Comment on the background quality.
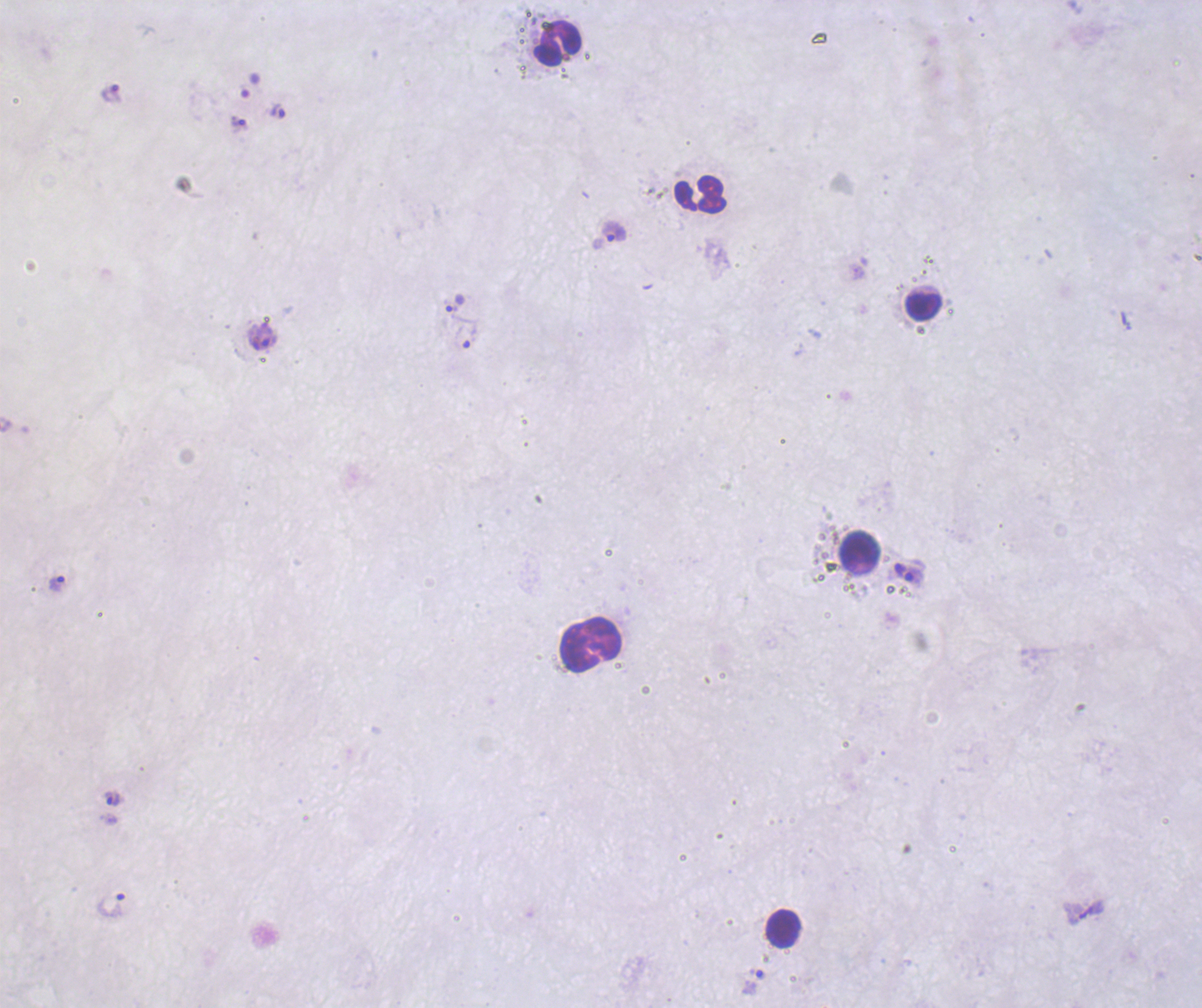
Unsatisfactory.

coordinate format = approximate centers as (x, y) in pixels
leukocyte locations = (557, 44), (701, 194), (924, 306), (859, 549), (590, 644), (783, 928)
trophozoite locations = (111, 93), (277, 111), (240, 125), (613, 232), (454, 304), (465, 331), (263, 337), (900, 569), (914, 577), (57, 583), (113, 799), (111, 905), (754, 981)
field of view = single
image size = 1202×1008 pixels
coloration quality = bad
result = Plasmodium parasites identified
preparation = thick blood film
magnification = 100x
context = previously used in an actual diagnosis
stain = Romanowsky